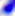

identification = Toxoplasma gondii
magnification = 400x
modality = photomicrograph